Assess this cell for malaria.
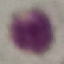

Uninfected.

Summary:
  - Image type: automatically extracted cell patch, resized to 64 × 64 pixels
  - Stain: Giemsa
  - Capture: smartphone through the microscope eyepiece
  - Preparation: thin blood film